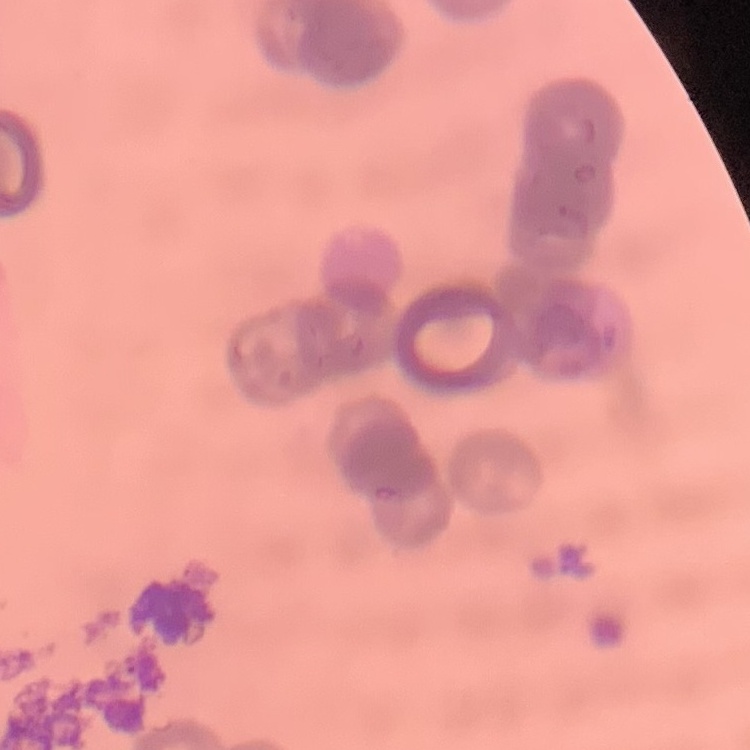

Summary:
  - Red blood cell morphology: rouleaux formation
  - Stain: Field's or Giemsa
  - Image type: square crop of a larger photomicrograph
  - Preparation: thin blood smear